Locate every malaria parasite.
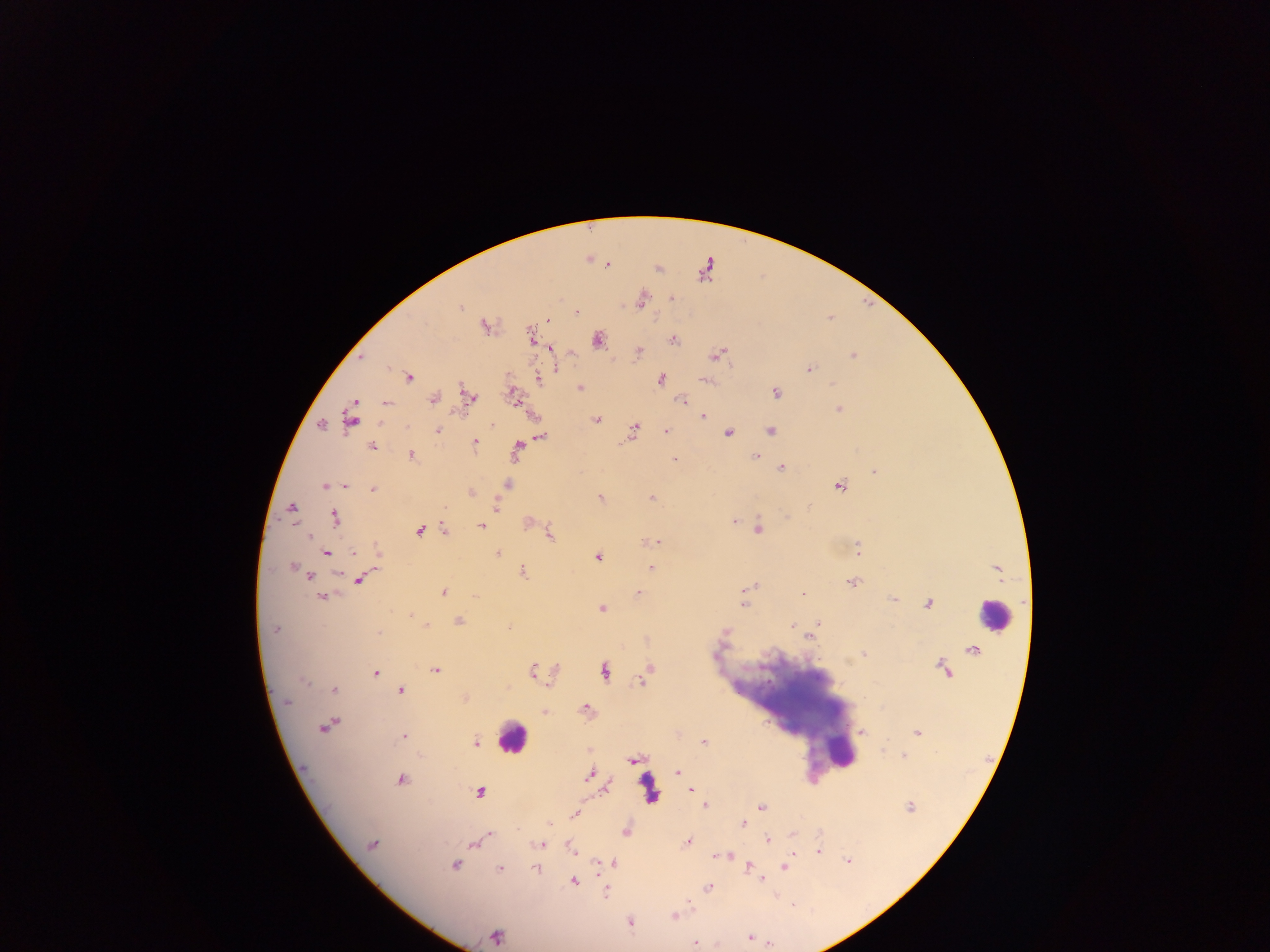

Approximate centers as x y in pixels.
Malaria parasites: 607 264; 672 298; 642 301; 460 308; 577 312; 548 320; 485 326; 533 337; 597 340; 672 340; 551 349; 638 353; 716 355; 853 356; 809 368; 556 369; 507 375; 408 377; 537 378; 661 379; 706 381; 580 388; 776 393; 514 395; 471 396; 434 399; 682 401; 386 402; 838 409; 703 416; 350 418; 596 419; 321 425; 492 425; 634 428; 438 431; 666 431; 770 431; 728 432; 541 437; 475 442; 371 447; 517 449; 411 455; 756 457; 674 459; 781 467; 874 472; 324 485; 344 485; 507 485; 839 485; 373 490; 471 493; 600 498; 652 498; 496 506; 292 508; 335 518; 734 521; 481 526; 445 529; 758 529; 419 530; 550 533; 657 541; 857 550; 327 553; 353 553; 378 554; 497 554; 597 557; 291 566; 651 568; 523 571; 309 577; 360 579; 853 583; 754 586; 638 592; 444 593; 804 593; 322 596; 893 599; 744 605; 928 605; 602 609; 410 614; 459 621; 818 623; 426 626; 791 626; 274 630; 727 631; 379 633; 809 638; 863 654; 435 671; 533 671; 646 671; 604 672; 375 673; 641 681; 304 682; 335 690; 400 691; 464 698; 287 701; 586 707; 544 712; 325 727; 861 732; 917 732; 403 737; 475 743; 704 743; 903 755; 631 761; 677 771; 589 775; 401 779; 691 791; 479 792; 705 806; 910 806; 761 807; 575 814; 550 823; 742 824; 625 832; 490 834; 792 834; 767 839; 687 842; 372 844; 541 844; 473 845; 819 850; 572 851; 792 854; 848 861; 614 863; 455 864; 784 866; 749 867; 500 869; 536 869; 599 874; 762 879; 574 881; 709 887; 606 893; 689 901; 674 916; 630 922; 495 937; 748 937; 695 943.

Summary:
  - Leukocyte locations: 993 614; 511 738; 841 752; 649 786
  - Country: Ghana
  - Preparation: thick blood smear
  - Capture: mobile-phone photograph through a microscope
  - Image size: 1270×952 pixels
  - Field of view: single